Identify the preparation type.
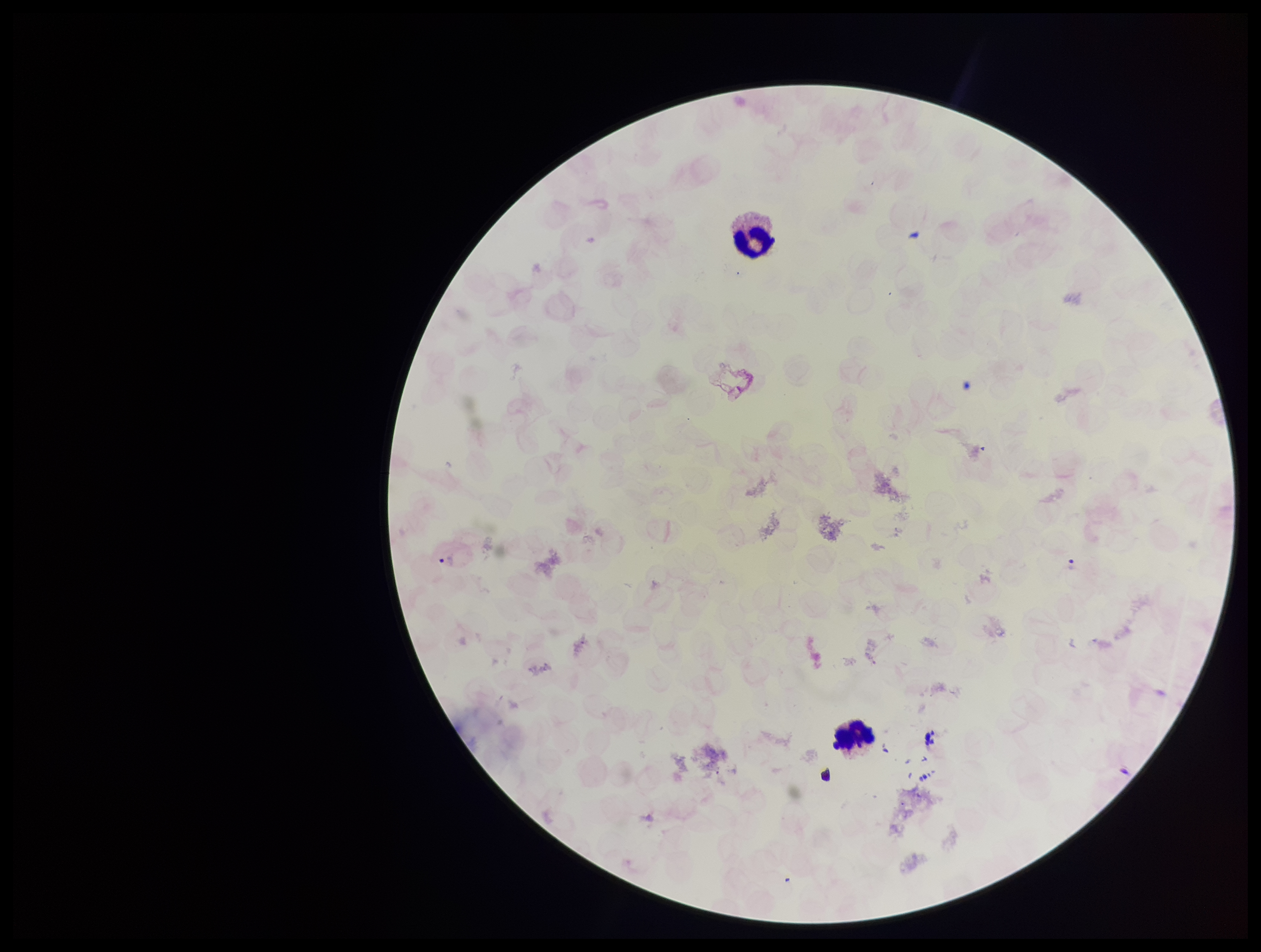

Thick.

patient malaria status = infected
parasite count = 1
field of view = one from this slide
Plasmodium parasites = detected
leukocyte count = 2
stain = Giemsa
image size = 1261×952 pixels
capture = smartphone photograph through the microscope eyepiece
species reported for this patient = Plasmodium vivax